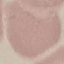
malaria status = uninfected
image type = cell patch, automatically extracted from a larger field of view and resized to 64 × 64 pixels
preparation = thin blood film
stain = Giemsa
capture = smartphone through the microscope eyepiece